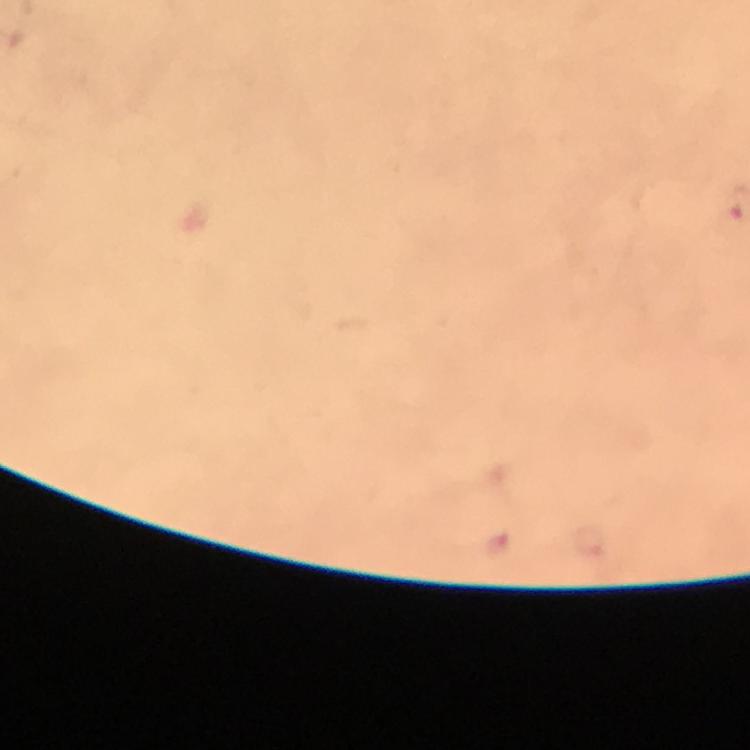

{
  "preparation": "thick smear",
  "immersion_oil": "applied",
  "stain": "Giemsa",
  "magnification": "100x",
  "context": "from a malaria diagnostic workup",
  "capture": "smartphone camera through the microscope",
  "image_size": "750×750 pixels",
  "cropped_from": "a single field of view",
  "malaria_parasite_locations": "approximate centers as (x, y) in pixels: (498, 543)"
}